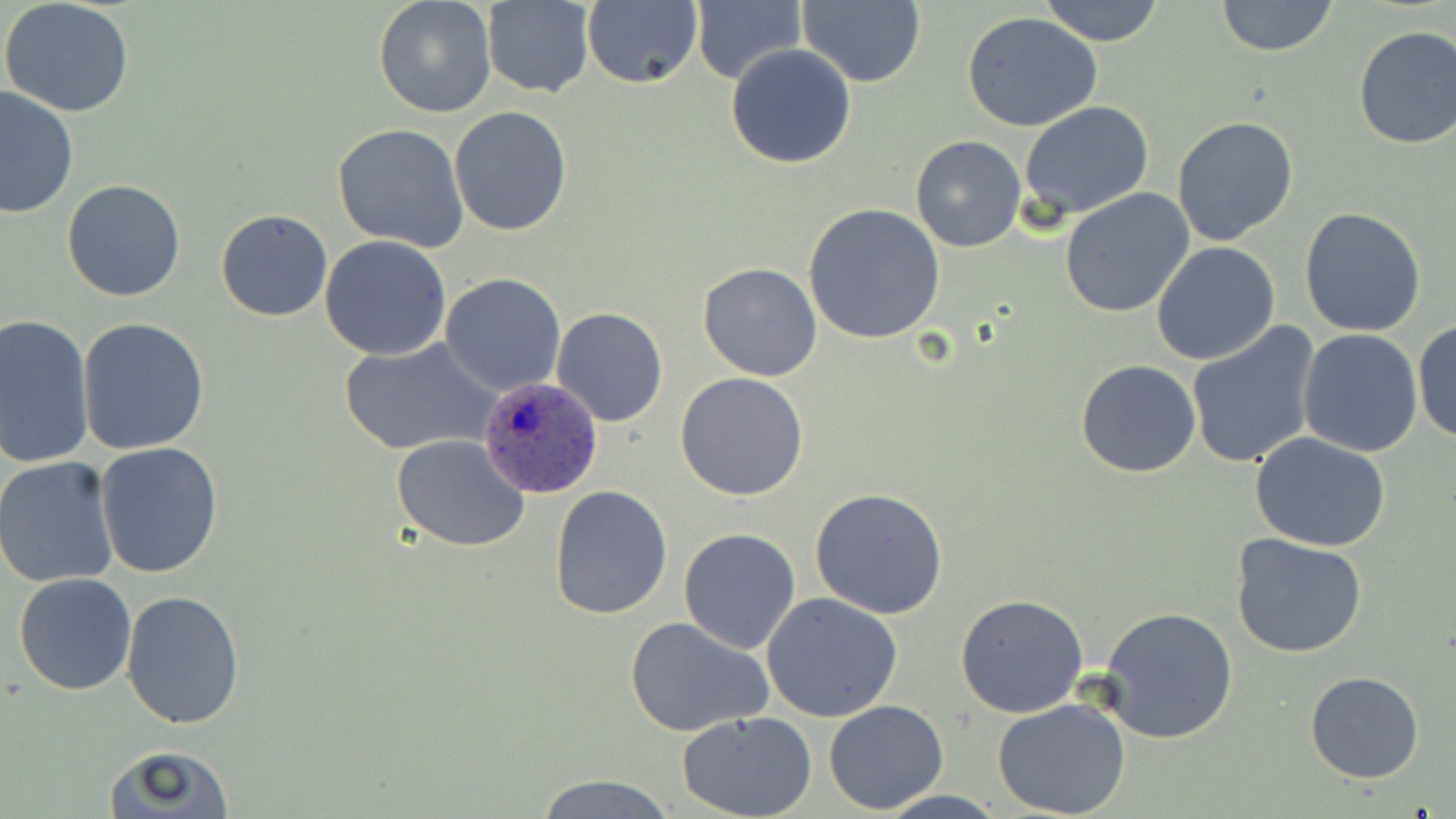

Approximate bounding boxes as (x1, y1, x2, y2) in pixels. Uninfected red blood cell locations: (373, 0, 497, 119), (798, 0, 926, 87), (1039, 0, 1166, 47), (0, 1, 135, 116), (582, 1, 703, 90), (691, 1, 806, 86), (1214, 1, 1340, 57), (482, 2, 595, 98), (963, 13, 1102, 133), (1352, 25, 1456, 150), (725, 44, 858, 169), (0, 83, 78, 219), (1019, 101, 1155, 219), (448, 106, 572, 236), (1170, 117, 1300, 249), (332, 123, 470, 252), (910, 135, 1026, 253), (62, 179, 186, 302), (1059, 188, 1196, 320), (804, 202, 947, 344), (1300, 206, 1426, 337), (215, 208, 333, 321), (319, 234, 452, 359), (1151, 241, 1281, 366), (697, 263, 823, 382), (440, 272, 566, 395), (551, 306, 669, 428), (0, 315, 96, 469), (75, 316, 209, 456), (1413, 319, 1455, 446), (1186, 320, 1322, 470), (1297, 330, 1424, 458), (340, 338, 498, 456), (1075, 360, 1202, 478), (675, 372, 809, 502), (391, 434, 530, 552), (1250, 434, 1391, 552), (95, 441, 224, 580), (1, 456, 119, 588), (548, 484, 673, 620), (808, 486, 951, 618), (677, 527, 802, 654), (1229, 534, 1370, 659), (13, 572, 138, 695), (120, 590, 247, 730), (761, 593, 903, 722), (956, 595, 1089, 719), (1097, 605, 1242, 745), (623, 615, 773, 739), (1305, 672, 1425, 784), (990, 697, 1135, 819), (823, 700, 949, 813), (676, 711, 817, 819), (102, 746, 237, 817), (536, 774, 675, 817). Plasmodium ovale-infected red blood cell locations: (479, 373, 602, 501). Slide-level diagnosis: Plasmodium ovale. Single field of view. Image is 1456×819 pixels. 1000x magnification. May-Grünwald-Giemsa stain. Light microscopy. Thin blood smear.